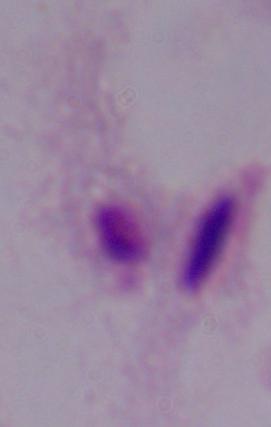
Photomicrograph. Captured at 1000x magnification. A trichomonad is seen.